Report the malaria status of this cell.
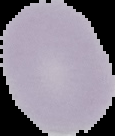
It is uninfected.

{
  "image_size": "115×136 pixels",
  "image_type": "cell region segmented out of the field of view; surrounding area masked to black",
  "preparation": "thin blood smear"
}